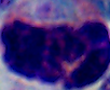 Micrograph. Captured at 1000x magnification. A leukocyte is shown.